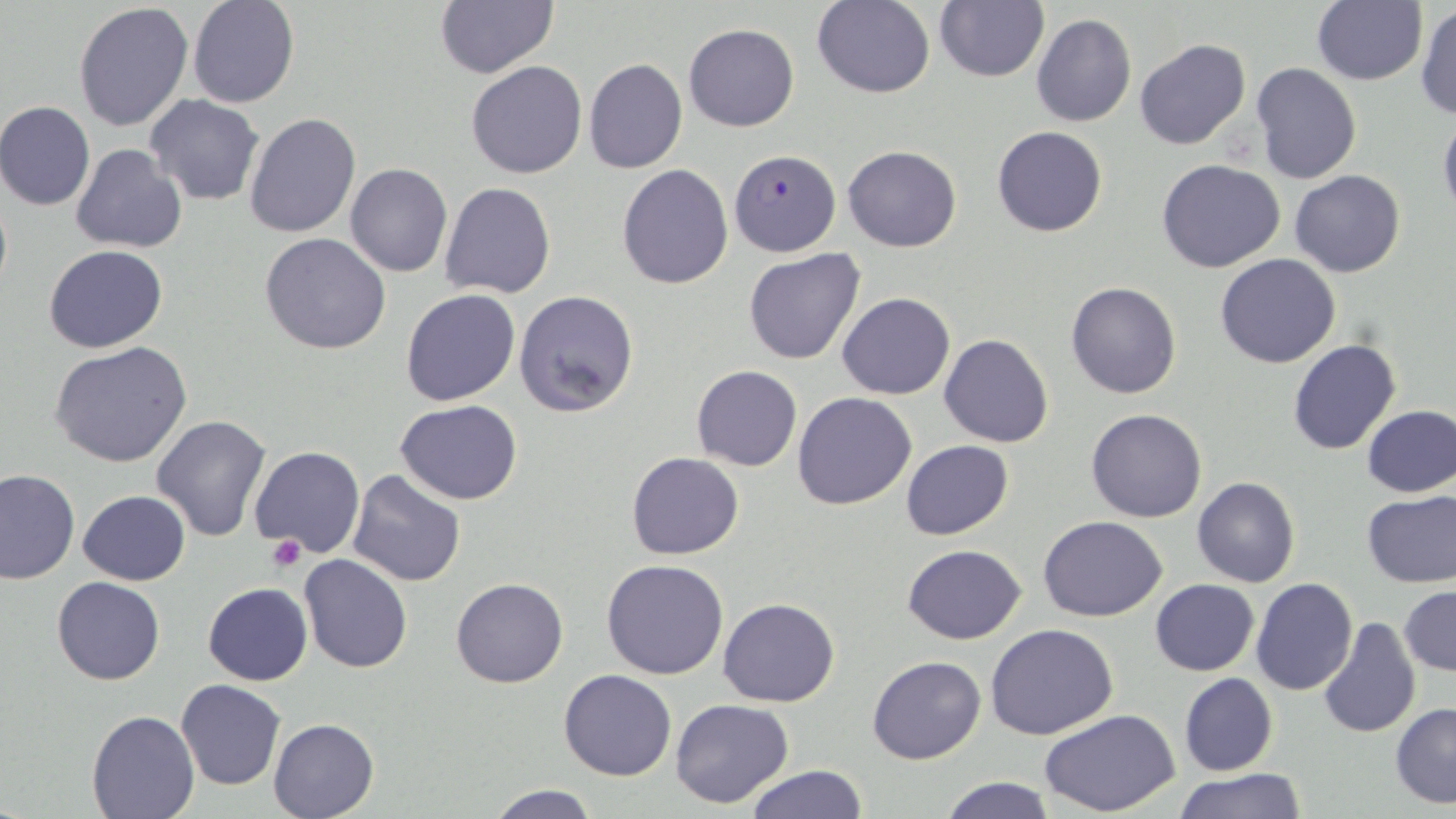
Summary:
  - Coordinate format: approximate bounding boxes as named x1/y1/x2/y2 corners in pixels
  - Plasmodium falciparum-infected red blood cell locations: (x1=731, y1=146, x2=837, y2=256)
  - Platelet locations: (x1=267, y1=533, x2=306, y2=573)
  - Uninfected red blood cell locations: (x1=812, y1=0, x2=934, y2=98), (x1=187, y1=1, x2=298, y2=108), (x1=434, y1=1, x2=559, y2=78), (x1=934, y1=1, x2=1048, y2=82), (x1=1311, y1=2, x2=1428, y2=85), (x1=73, y1=3, x2=195, y2=132), (x1=1416, y1=3, x2=1456, y2=120), (x1=1030, y1=12, x2=1137, y2=127), (x1=684, y1=23, x2=799, y2=131), (x1=1135, y1=37, x2=1250, y2=149), (x1=583, y1=59, x2=687, y2=173), (x1=467, y1=60, x2=587, y2=178), (x1=1251, y1=62, x2=1360, y2=184), (x1=145, y1=94, x2=265, y2=206), (x1=0, y1=101, x2=95, y2=211), (x1=1438, y1=110, x2=1456, y2=224), (x1=244, y1=112, x2=361, y2=238), (x1=992, y1=126, x2=1107, y2=237), (x1=70, y1=144, x2=188, y2=253), (x1=842, y1=145, x2=962, y2=251), (x1=1158, y1=159, x2=1287, y2=274), (x1=345, y1=164, x2=453, y2=278), (x1=616, y1=164, x2=734, y2=289), (x1=1290, y1=170, x2=1405, y2=277), (x1=440, y1=182, x2=557, y2=299), (x1=260, y1=233, x2=391, y2=355), (x1=43, y1=245, x2=168, y2=352), (x1=744, y1=249, x2=866, y2=364), (x1=1215, y1=254, x2=1341, y2=369), (x1=1066, y1=282, x2=1182, y2=400), (x1=401, y1=289, x2=522, y2=407), (x1=513, y1=290, x2=639, y2=417), (x1=837, y1=292, x2=956, y2=400), (x1=939, y1=334, x2=1054, y2=447), (x1=1287, y1=338, x2=1401, y2=455), (x1=50, y1=342, x2=192, y2=468), (x1=691, y1=365, x2=801, y2=470), (x1=792, y1=391, x2=919, y2=510), (x1=395, y1=398, x2=522, y2=504), (x1=1360, y1=404, x2=1456, y2=497), (x1=1086, y1=408, x2=1207, y2=524), (x1=151, y1=413, x2=272, y2=542), (x1=901, y1=439, x2=1013, y2=540), (x1=250, y1=446, x2=366, y2=559), (x1=628, y1=452, x2=744, y2=559), (x1=0, y1=468, x2=79, y2=584), (x1=348, y1=470, x2=469, y2=586), (x1=1202, y1=475, x2=1315, y2=693), (x1=1192, y1=477, x2=1300, y2=588), (x1=78, y1=489, x2=190, y2=585), (x1=1361, y1=489, x2=1456, y2=588), (x1=1039, y1=516, x2=1168, y2=620), (x1=903, y1=544, x2=1027, y2=643), (x1=298, y1=555, x2=414, y2=674), (x1=601, y1=558, x2=729, y2=679), (x1=52, y1=576, x2=165, y2=686), (x1=450, y1=576, x2=568, y2=688), (x1=1250, y1=578, x2=1358, y2=696), (x1=1150, y1=579, x2=1260, y2=676), (x1=203, y1=583, x2=313, y2=685), (x1=1399, y1=585, x2=1456, y2=676), (x1=718, y1=597, x2=839, y2=708), (x1=1317, y1=618, x2=1420, y2=737), (x1=985, y1=623, x2=1118, y2=739), (x1=868, y1=656, x2=986, y2=765), (x1=558, y1=669, x2=677, y2=781), (x1=1179, y1=673, x2=1278, y2=777), (x1=175, y1=678, x2=285, y2=790), (x1=669, y1=698, x2=794, y2=809), (x1=1391, y1=703, x2=1456, y2=809), (x1=86, y1=710, x2=198, y2=819), (x1=1041, y1=711, x2=1181, y2=817), (x1=268, y1=718, x2=378, y2=819), (x1=745, y1=763, x2=869, y2=819), (x1=1175, y1=768, x2=1305, y2=819), (x1=936, y1=776, x2=1057, y2=818), (x1=485, y1=783, x2=601, y2=818)
  - Slide-level diagnosis: Plasmodium falciparum
  - Field of view: single
  - Preparation: thin blood film
  - Stain: May-Grünwald-Giemsa
  - Magnification: 1000x
  - Image size: 1456×819 pixels
  - Modality: light microscopy